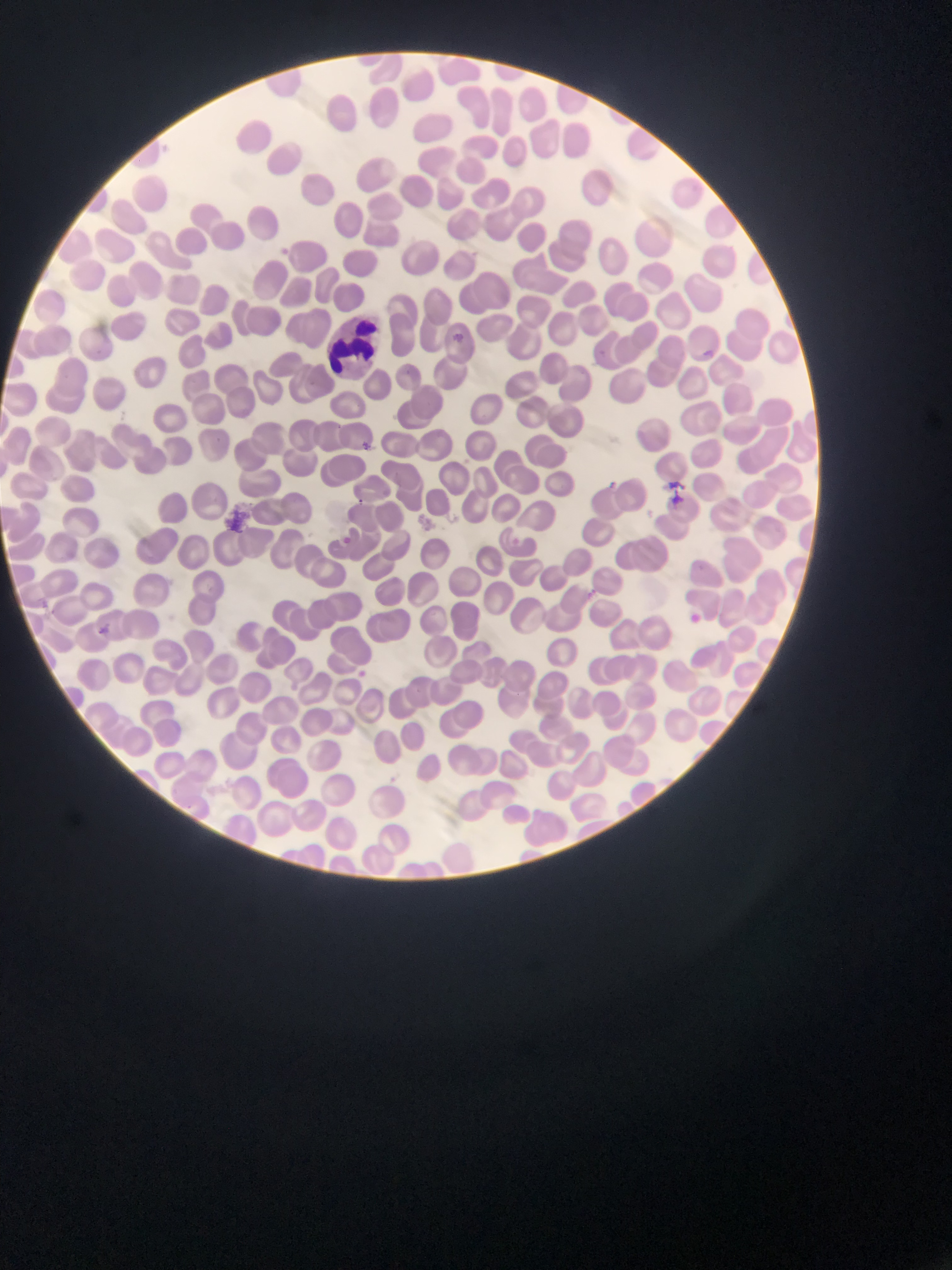
Approximate bounding boxes as {left, top, right, bottom} in pixels.
Summary:
  - Leukocyte locations: {327, 317, 393, 379}
  - Plasmodium parasite locations: {279, 242, 306, 274}, {446, 327, 465, 350}, {702, 340, 717, 369}, {361, 433, 377, 454}, {598, 469, 625, 496}, {661, 476, 689, 504}, {335, 527, 355, 544}, {503, 535, 527, 553}, {28, 593, 53, 618}, {684, 604, 706, 624}, {96, 620, 108, 639}, {359, 667, 372, 684}
  - Image size: 952×1270 pixels
  - Field of view: single
  - Capture: mobile-phone photograph through a microscope
  - Country: Ghana
  - Preparation: thin blood smear